Give the preparation type.
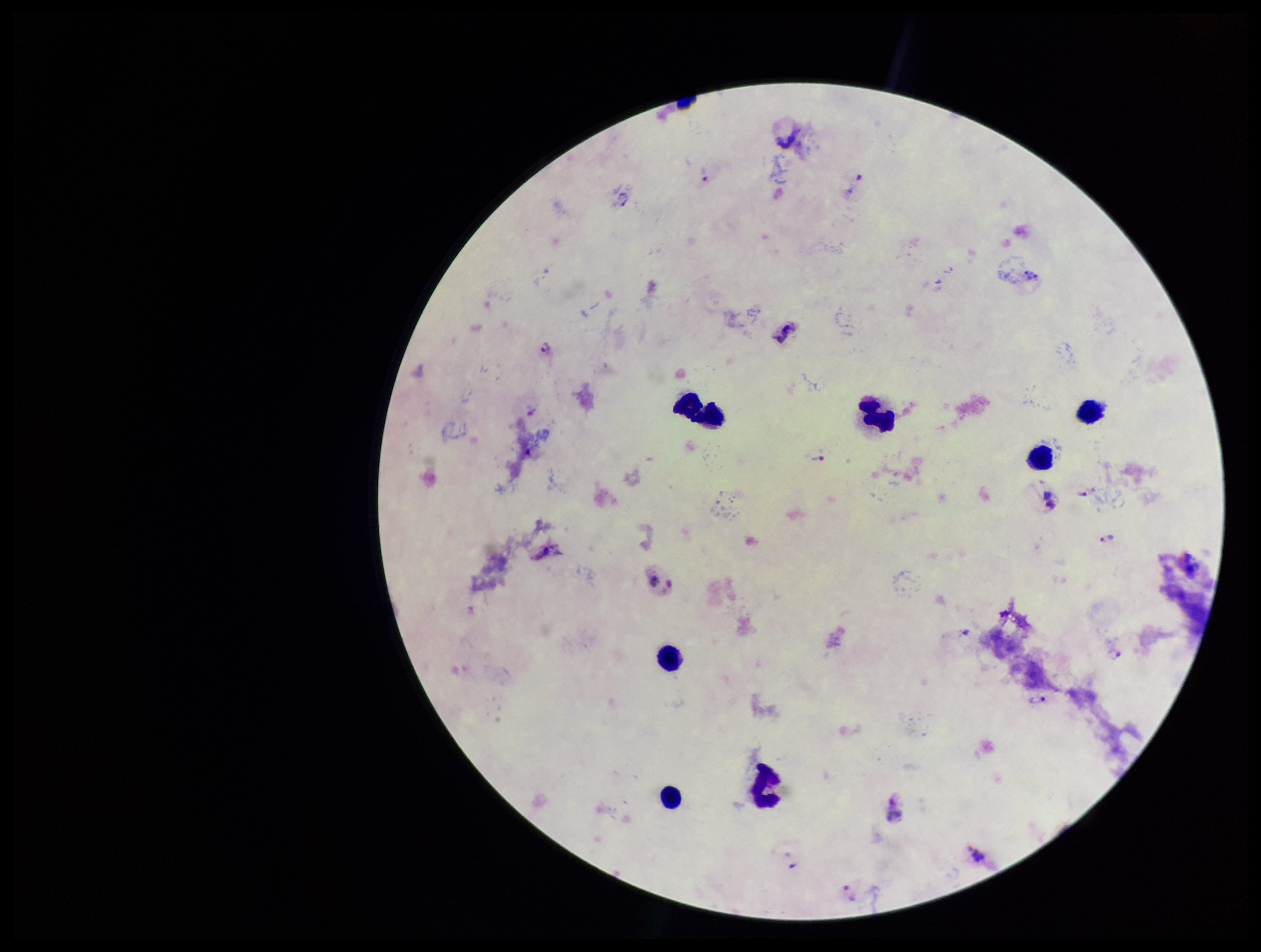
It is a thick blood smear.

patient malaria status = infected
Plasmodium parasites = detected
field of view = one from this slide
stain = Giemsa
parasite count = 9
image size = 1261×952 pixels
species reported for this patient = Plasmodium vivax
capture = smartphone photograph through the microscope eyepiece
leukocyte count = 7